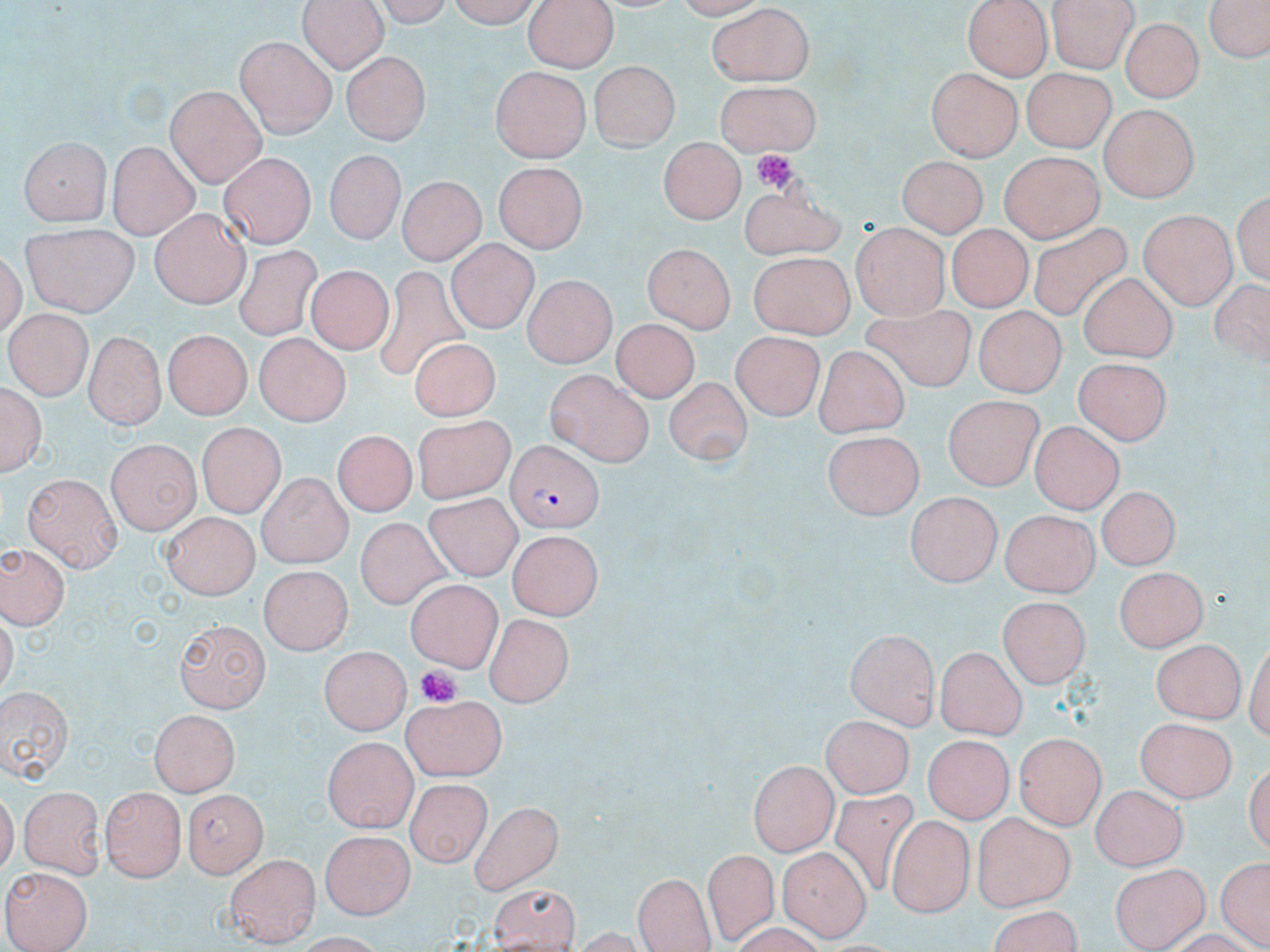
Plasmodium falciparum-infected red blood cell locations = approximate bounding boxes as (x1,y1)-(x2,y2) corner pairs in pixels: (504,443)-(603,534)
slide-level diagnosis = Plasmodium falciparum
image size = 1270×952 pixels
magnification = 1000x
field of view = one of a larger specimen
preparation = thin blood film
stain = May-Grünwald-Giemsa
modality = optical microscopy
platelet locations = approximate bounding boxes as (x1,y1)-(x2,y2) corner pairs in pixels: (751,150)-(796,196), (415,666)-(459,709)
uninfected red blood cell locations = approximate bounding boxes as (x1,y1)-(x2,y2) corner pairs in pixels: (295,0)-(387,73), (446,0)-(546,29), (521,0)-(621,72), (962,0)-(1053,80), (1207,0)-(1269,66), (1049,2)-(1136,72), (706,4)-(816,85), (948,13)-(1038,132), (1123,17)-(1203,103), (236,36)-(341,135), (340,54)-(426,144), (588,62)-(679,152), (488,65)-(589,161), (926,67)-(1024,158), (1020,67)-(1116,150), (710,76)-(820,158), (166,85)-(265,184), (1100,104)-(1195,201), (17,135)-(111,226), (656,139)-(744,227), (107,140)-(199,238), (325,150)-(401,245), (997,150)-(1101,243), (220,152)-(313,248), (895,156)-(989,245), (492,157)-(588,246), (399,175)-(485,266), (735,190)-(851,260), (1233,190)-(1268,290), (147,210)-(246,307), (1138,211)-(1235,309), (21,224)-(137,317), (850,224)-(951,319), (1025,225)-(1134,323), (945,226)-(1035,311), (446,238)-(542,337), (642,243)-(737,332), (233,247)-(319,342), (748,252)-(851,340), (307,263)-(394,357), (375,265)-(469,376), (1079,271)-(1179,363), (524,273)-(613,368), (973,308)-(1068,395), (5,310)-(89,400), (862,310)-(976,392), (613,318)-(697,401), (86,329)-(166,432), (159,331)-(256,421), (255,332)-(352,428), (732,333)-(827,421), (407,336)-(501,420), (813,345)-(908,438), (1073,357)-(1171,446), (544,367)-(655,464), (662,376)-(751,465), (1,382)-(46,480), (943,398)-(1046,487), (408,415)-(513,503), (1029,419)-(1124,513), (194,422)-(290,513), (328,430)-(424,515), (822,433)-(927,519), (107,439)-(200,534), (253,473)-(351,569), (20,476)-(122,568), (1095,486)-(1180,571), (902,491)-(1001,586), (422,493)-(526,583), (1000,508)-(1097,596), (161,512)-(260,596), (355,515)-(446,608), (510,530)-(604,620), (2,543)-(70,628), (260,563)-(350,657), (1115,564)-(1209,653), (407,577)-(500,671), (995,591)-(1088,688), (483,610)-(573,706), (173,620)-(268,711), (845,629)-(940,727), (1151,638)-(1246,721), (937,643)-(1030,737), (321,647)-(410,734), (0,683)-(74,782), (401,694)-(503,780), (149,708)-(240,796), (820,713)-(912,797), (1137,716)-(1234,804), (1013,732)-(1109,828), (324,734)-(415,831), (924,737)-(1014,823), (746,761)-(837,853), (405,778)-(491,862), (21,784)-(106,876), (1090,785)-(1187,871), (102,786)-(185,880), (183,789)-(269,876), (826,791)-(926,894), (469,801)-(565,895), (205,810)-(302,932), (971,814)-(1073,909), (887,815)-(970,917), (321,830)-(414,919), (777,847)-(870,939), (703,848)-(775,940), (226,853)-(319,943), (1215,855)-(1268,950), (1110,861)-(1212,949), (4,866)-(93,951), (634,873)-(714,952), (488,883)-(582,952), (988,903)-(1091,952)